Name the cell type shown.
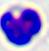
A leukocyte.

Summary:
  - Modality: micrograph
  - Magnification: 400x